Locate and identify every blood parasite.
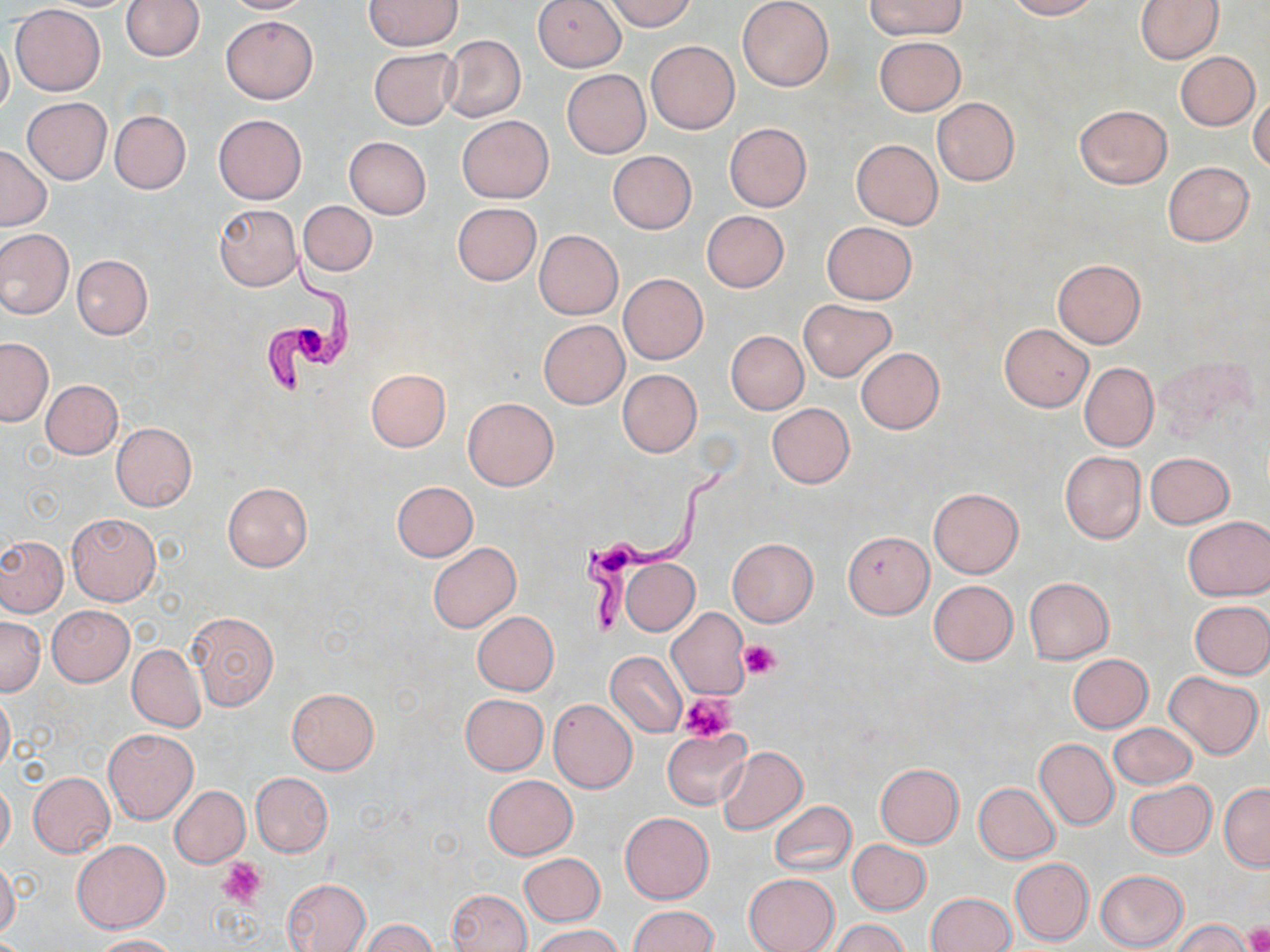

Approximate bounding boxes as [x1, y1, x2, y2] in pixels.
Trypanosoma brucei: [261, 242, 360, 397], [580, 465, 725, 636].
No Plasmodium falciparum, Plasmodium ovale, Plasmodium malariae, Plasmodium vivax, or Babesia divergens observed.

slide-level diagnosis = Trypanosoma brucei
preparation = thin blood film
stain = May-Grünwald-Giemsa
field of view = one of a larger specimen
uninfected red blood cell locations = approximate bounding boxes as [x1, y1, x2, y2] in pixels: [120, 0, 204, 60], [221, 0, 311, 13], [533, 0, 626, 72], [604, 0, 695, 32], [737, 0, 834, 91], [865, 0, 966, 39], [1005, 0, 1097, 19], [1134, 0, 1223, 63], [364, 1, 462, 50], [11, 5, 106, 95], [220, 15, 318, 104], [0, 32, 13, 121], [440, 35, 525, 122], [875, 35, 965, 115], [646, 41, 739, 133], [369, 48, 459, 130], [1176, 52, 1260, 130], [562, 70, 650, 158], [1249, 90, 1270, 174], [23, 98, 112, 183], [931, 98, 1019, 186], [1073, 104, 1172, 188], [109, 110, 191, 194], [212, 114, 306, 205], [456, 115, 553, 202], [723, 122, 811, 212], [344, 137, 430, 219], [851, 139, 943, 229], [0, 144, 51, 230], [607, 150, 696, 232], [1164, 161, 1253, 246], [299, 200, 376, 277], [452, 202, 541, 285], [213, 204, 302, 291], [702, 210, 789, 292], [822, 221, 917, 304], [0, 229, 73, 319], [535, 230, 622, 319], [71, 255, 153, 339], [1053, 259, 1145, 348], [617, 273, 709, 364], [799, 299, 896, 381], [538, 320, 629, 408], [1000, 324, 1093, 411], [726, 331, 808, 413], [0, 338, 52, 426], [855, 347, 944, 433], [1079, 362, 1158, 451], [366, 368, 451, 451], [616, 369, 703, 457], [41, 379, 122, 458], [463, 398, 558, 490], [767, 403, 854, 487], [111, 422, 196, 510], [1060, 450, 1146, 543], [1145, 452, 1234, 528], [391, 481, 478, 561], [222, 482, 311, 572], [927, 488, 1024, 578], [67, 512, 160, 606], [1182, 515, 1269, 600], [842, 531, 934, 618], [0, 535, 67, 616], [726, 538, 818, 627], [428, 542, 520, 631], [621, 559, 699, 635], [1024, 577, 1113, 663], [929, 580, 1018, 665], [1190, 599, 1270, 678], [47, 606, 134, 686], [666, 607, 751, 700], [187, 610, 279, 710], [472, 611, 559, 695], [0, 617, 44, 695], [127, 644, 206, 731], [606, 652, 686, 736], [1067, 654, 1153, 733], [1164, 671, 1263, 759], [287, 688, 378, 773], [0, 689, 14, 774], [460, 694, 548, 774], [548, 699, 637, 794], [1108, 722, 1197, 789], [104, 728, 197, 823], [661, 728, 750, 809], [1034, 738, 1118, 830], [716, 746, 807, 835], [874, 763, 964, 847], [27, 772, 115, 857], [250, 772, 333, 857], [483, 775, 577, 859], [0, 777, 14, 857], [1124, 780, 1216, 859], [974, 782, 1061, 864], [1219, 783, 1270, 870], [171, 786, 250, 866], [770, 801, 857, 877], [620, 813, 714, 903], [72, 839, 170, 932], [848, 840, 931, 915], [519, 853, 604, 925], [0, 858, 20, 942], [1010, 858, 1094, 945], [1095, 870, 1189, 951], [743, 873, 839, 952], [282, 878, 371, 952], [446, 889, 531, 952], [927, 893, 1015, 952], [628, 905, 717, 952], [360, 919, 436, 952], [830, 919, 909, 952], [1172, 919, 1255, 952], [532, 925, 624, 952], [91, 934, 180, 952]
platelet locations = approximate bounding boxes as [x1, y1, x2, y2] in pixels: [738, 641, 780, 679], [678, 695, 736, 741], [219, 859, 267, 908], [1243, 925, 1270, 952]
modality = light microscopy
image size = 1270×952 pixels
magnification = 1000x